Name the parasite shown.
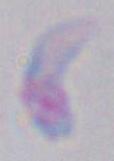

Toxoplasma gondii.

{
  "modality": "micrograph",
  "magnification": "1000x"
}